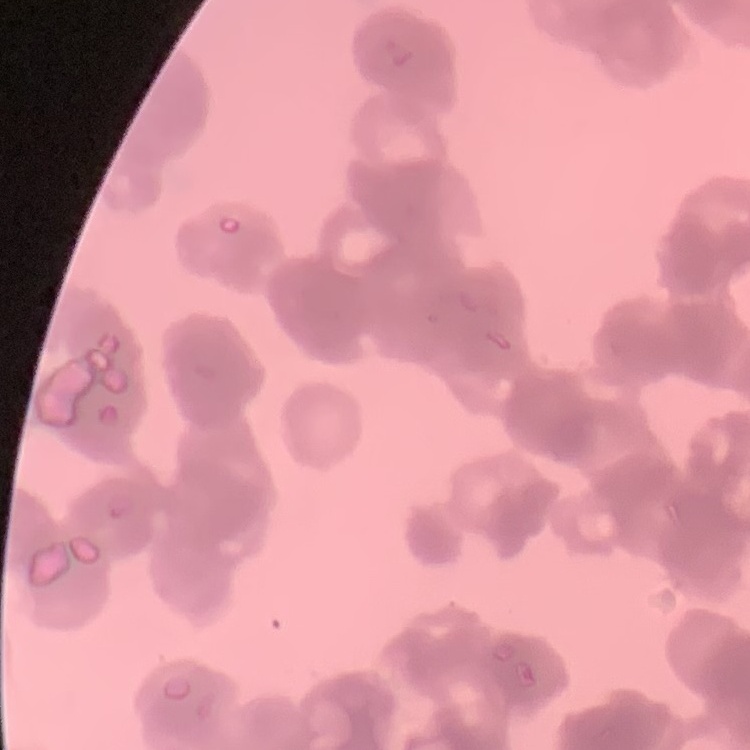
{
  "red_blood_cell_morphology": "rouleaux formation",
  "stain": "Field's or Giemsa",
  "preparation": "thin blood film",
  "image_type": "square crop of a larger photomicrograph"
}